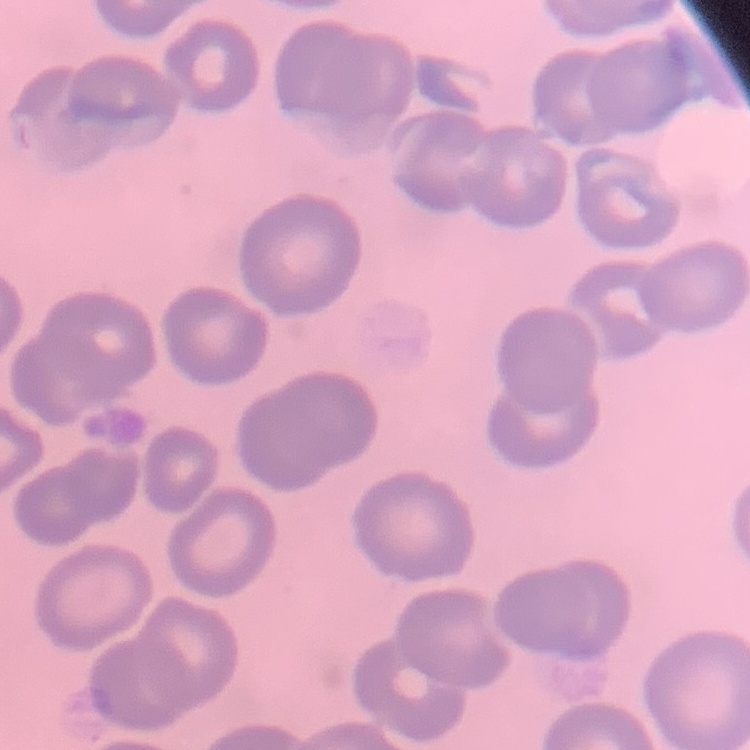
The erythrocytes exhibit no rouleaux formation. Thin blood film. One tile cut from a larger photomicrograph. Stained with either Field's or Giemsa.